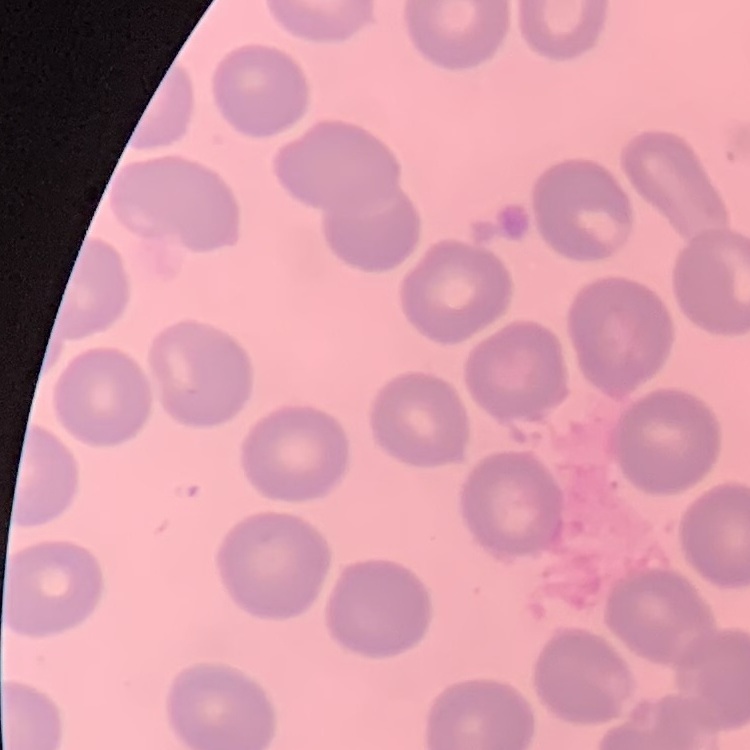
{
  "red_blood_cell_morphology": "no rouleaux formation",
  "image_type": "one tile cut from a larger photomicrograph",
  "stain": "Field's or Giemsa",
  "preparation": "thin blood smear"
}